Outline each uninfected red blood cell.
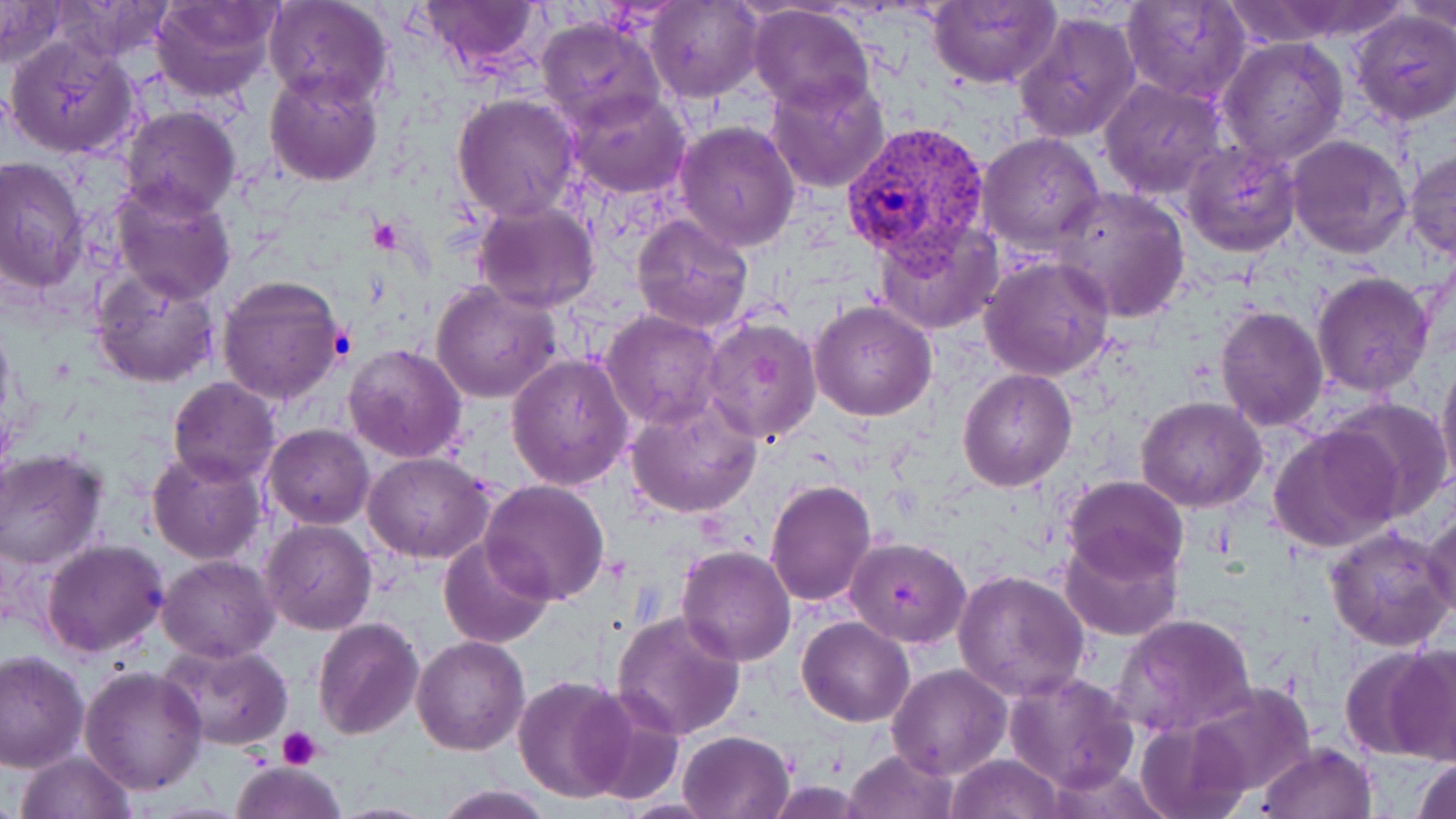

Approximate bounding boxes as [x1, y1, x2, y2] in pixels.
Uninfected red blood cells: [151, 0, 279, 102], [263, 0, 395, 111], [418, 0, 545, 73], [928, 0, 1060, 90], [1122, 0, 1250, 103], [0, 1, 65, 69], [49, 1, 180, 64], [647, 1, 761, 101], [748, 1, 876, 114], [1401, 1, 1456, 34], [1349, 9, 1456, 126], [1013, 11, 1141, 145], [537, 15, 663, 129], [6, 35, 139, 159], [1218, 38, 1349, 168], [263, 68, 382, 187], [766, 71, 891, 193], [1100, 79, 1228, 200], [563, 88, 693, 199], [451, 93, 582, 222], [119, 106, 241, 220], [675, 120, 800, 250], [978, 132, 1105, 253], [1288, 134, 1413, 258], [1183, 140, 1302, 258], [1405, 150, 1456, 259], [0, 157, 88, 291], [109, 180, 236, 303], [1052, 187, 1191, 321], [474, 201, 600, 311], [631, 213, 756, 335], [873, 219, 1003, 334], [978, 254, 1117, 382], [91, 266, 223, 389], [1313, 272, 1435, 395], [215, 273, 346, 408], [429, 279, 561, 405], [810, 300, 938, 421], [1215, 304, 1327, 430], [601, 311, 724, 428], [699, 316, 822, 447], [343, 343, 468, 465], [507, 354, 634, 489], [1437, 356, 1456, 492], [957, 369, 1077, 491], [167, 377, 280, 486], [1136, 397, 1267, 513], [1328, 397, 1452, 519], [626, 399, 761, 519], [265, 424, 374, 528], [1269, 424, 1404, 554], [0, 449, 110, 572], [147, 449, 266, 564], [363, 452, 495, 562], [1063, 475, 1187, 586], [479, 479, 611, 605], [765, 479, 878, 607], [1423, 507, 1456, 621], [261, 520, 376, 636], [1325, 523, 1456, 652], [1061, 529, 1182, 642], [437, 535, 555, 649], [846, 537, 972, 649], [40, 539, 169, 659], [677, 546, 796, 664], [157, 554, 279, 662], [954, 568, 1091, 702], [612, 610, 745, 739], [1113, 612, 1257, 739], [312, 615, 423, 739], [798, 616, 915, 727], [410, 637, 529, 756], [160, 642, 294, 751], [1380, 646, 1456, 763], [0, 650, 88, 771], [887, 664, 1011, 780], [79, 667, 207, 796], [1004, 668, 1140, 792], [513, 676, 633, 803], [1181, 680, 1318, 801], [573, 692, 687, 807], [1135, 718, 1249, 819], [677, 729, 797, 819], [1258, 741, 1375, 819], [846, 748, 957, 819], [15, 750, 139, 819], [946, 752, 1065, 819], [1411, 757, 1456, 819], [229, 758, 345, 819], [433, 784, 554, 819].

Platelet locations: [371, 216, 402, 252], [278, 727, 321, 771]. Plasmodium vivax-infected red blood cell locations: [840, 120, 992, 280]. Slide-level diagnosis: Plasmodium vivax. 1000x magnification. Single field of view. Image is 1456×819 pixels. May-Grünwald-Giemsa-stained preparation. Optical microscopy. Thin blood film.